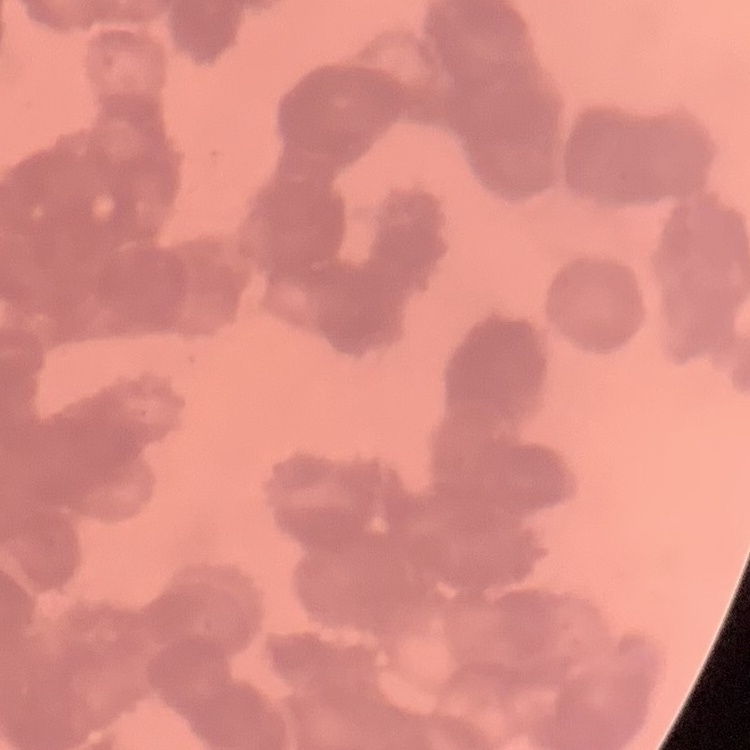 The red blood cells exhibit rouleaux formation. One tile cut from a larger photomicrograph. Field's or Giemsa stain. Thin blood film.